Assess this cell for malaria.
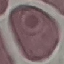
It is uninfected.

image type = automatically extracted cell patch, resized to 64 × 64 pixels
preparation = thin blood film
capture = smartphone camera at the microscope eyepiece
stain = Giemsa